Report the malaria status of this cell.
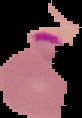

It is parasitized.

Summary:
  - Preparation: thin blood film
  - Image size: 82×118 pixels
  - Image type: segmented cell region with the area outside set to black